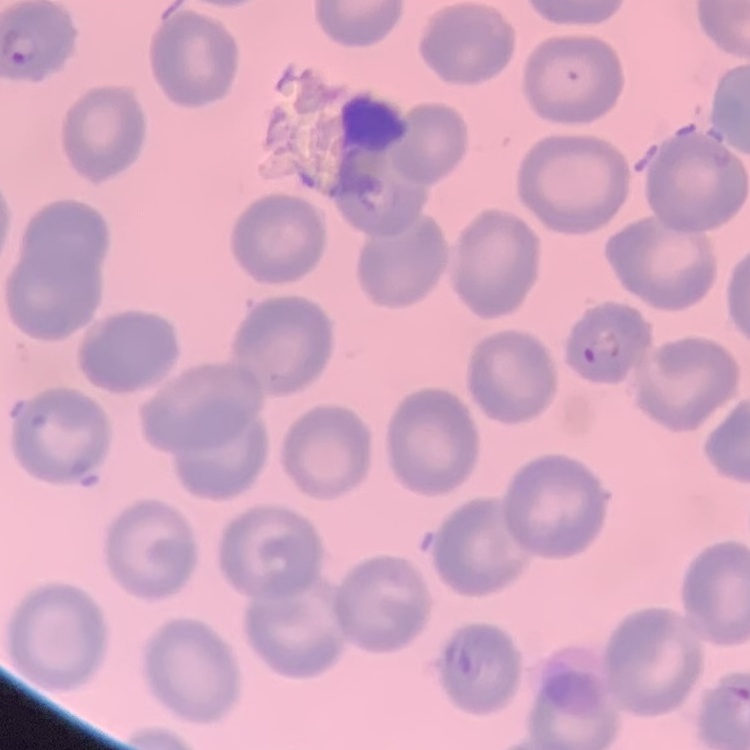

{
  "erythrocyte_morphology": "no rouleaux formation",
  "preparation": "thin blood smear",
  "image_type": "one tile cut from a larger photomicrograph",
  "stain": "Field's or Giemsa"
}